State which parasite is depicted.
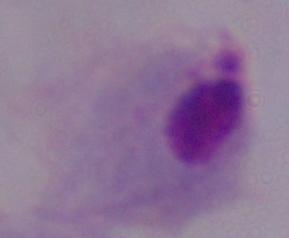

This is a trichomonad.

Photomicrograph. 1000x magnification.